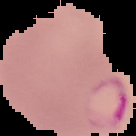
preparation = thin blood smear
image size = 136×136 pixels
malaria status = parasitized
image type = segmented cell region with the area outside set to black